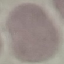
Summary:
  - Result: no malaria parasites detected
  - Capture: smartphone camera at the microscope eyepiece
  - Stain: Giemsa
  - Preparation: thin blood smear
  - Image type: cell patch, automatically extracted from a larger field of view and resized to 64 × 64 pixels